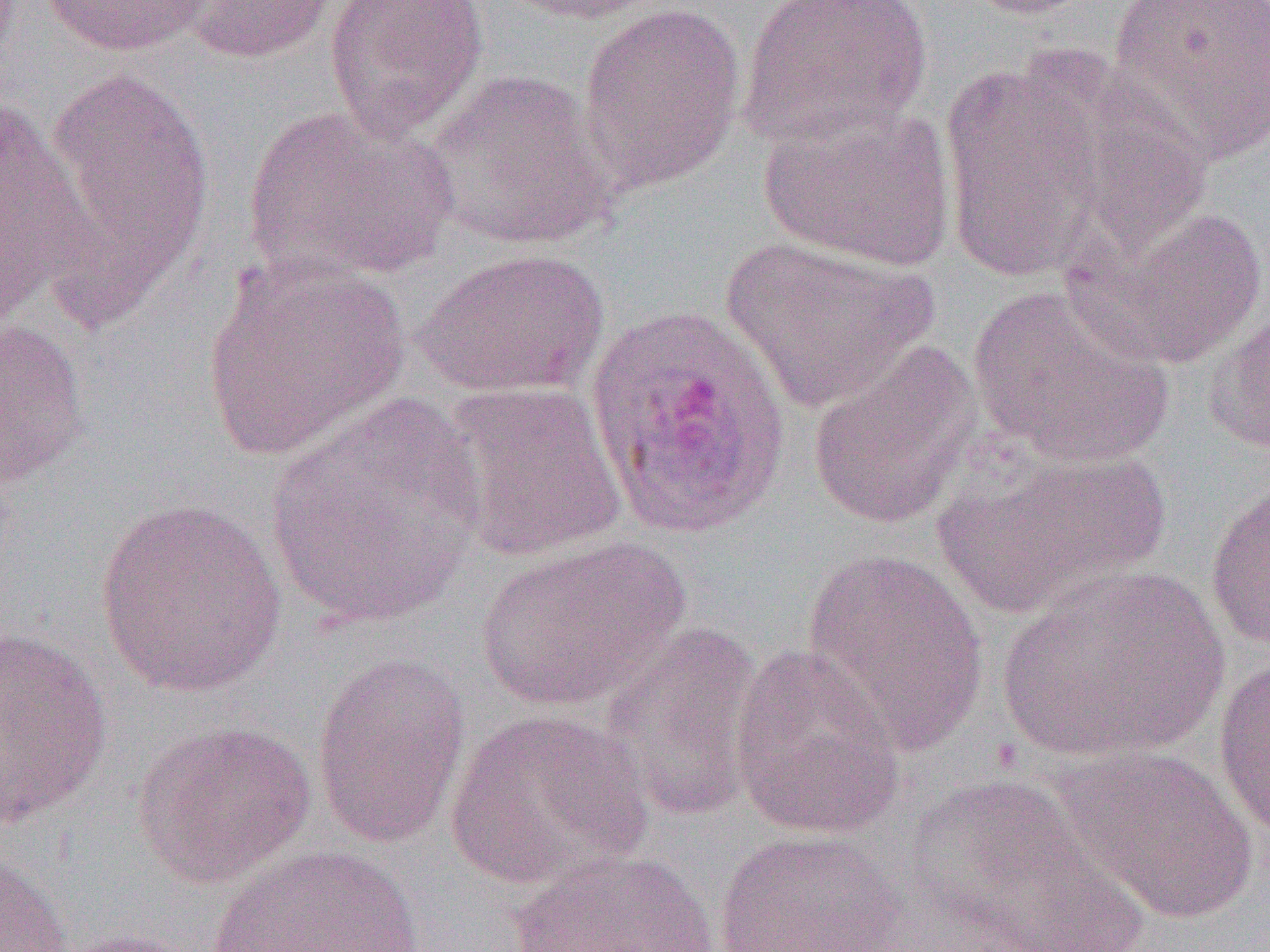
Approximate bounding boxes as (x1,y1)-(x2,y2) corner pairs in pixels. Plasmodium ovale-infected red blood cell locations: (584,304)-(794,541). Uninfected red blood cell locations: (39,0)-(212,57), (177,0)-(339,64), (323,0)-(490,143), (493,0)-(668,25), (736,0)-(933,149), (954,0)-(1104,20), (1106,0)-(1270,164), (577,3)-(748,194), (1008,51)-(1212,254), (940,60)-(1113,287), (45,64)-(215,293), (420,69)-(619,251), (0,94)-(98,327), (757,100)-(955,271), (242,105)-(457,287), (1075,203)-(1268,369), (720,236)-(938,414), (413,247)-(611,399), (201,253)-(412,463), (967,283)-(1176,468), (1204,292)-(1270,458), (0,317)-(91,488), (805,340)-(983,531), (438,380)-(628,561), (265,395)-(488,632), (935,446)-(1172,618), (1204,473)-(1270,652), (93,496)-(289,699), (472,535)-(689,712), (799,547)-(991,755), (997,565)-(1228,763), (598,621)-(766,823), (0,625)-(113,828), (728,643)-(907,840), (1213,649)-(1270,843), (311,651)-(471,850), (443,709)-(653,892), (132,719)-(316,889), (1051,746)-(1260,924), (895,775)-(1148,952), (712,829)-(908,952), (206,844)-(428,952), (503,848)-(730,952), (0,850)-(74,951), (51,929)-(201,952). Slide-level diagnosis: Plasmodium ovale. One field of a larger specimen. Image is 1270×952 pixels. 1000x magnification. Light microscopy. Thin blood smear.